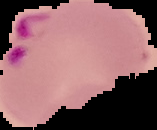

Summary:
  - Preparation: thin blood smear
  - Image size: 157×130 pixels
  - Malaria status: parasitized
  - Image type: segmented cell region on a black background